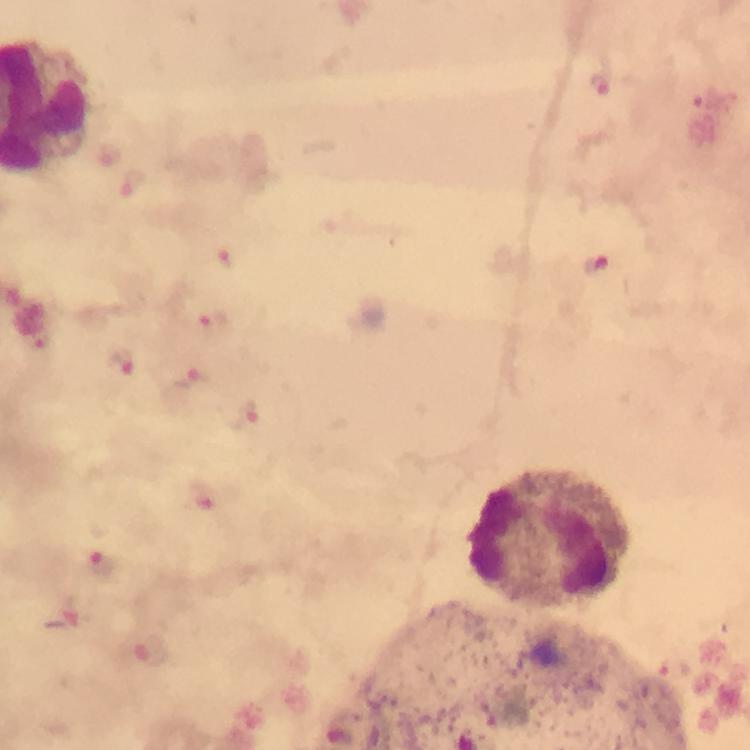

Approximate centers as (x, y) in pixels.
Summary:
  - Plasmodium parasite locations: (105, 566), (157, 648)
  - Leukocyte locations: (549, 538)
  - Image size: 750×750 pixels
  - Cropped from: one field of view
  - Stain: Giemsa
  - Capture: smartphone camera through the microscope
  - Immersion oil: applied
  - Preparation: thick blood film
  - Context: from a malaria diagnostic workup
  - Magnification: 100x